Name the parasite shown.
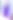

Toxoplasma gondii.

400x magnification. Micrograph.